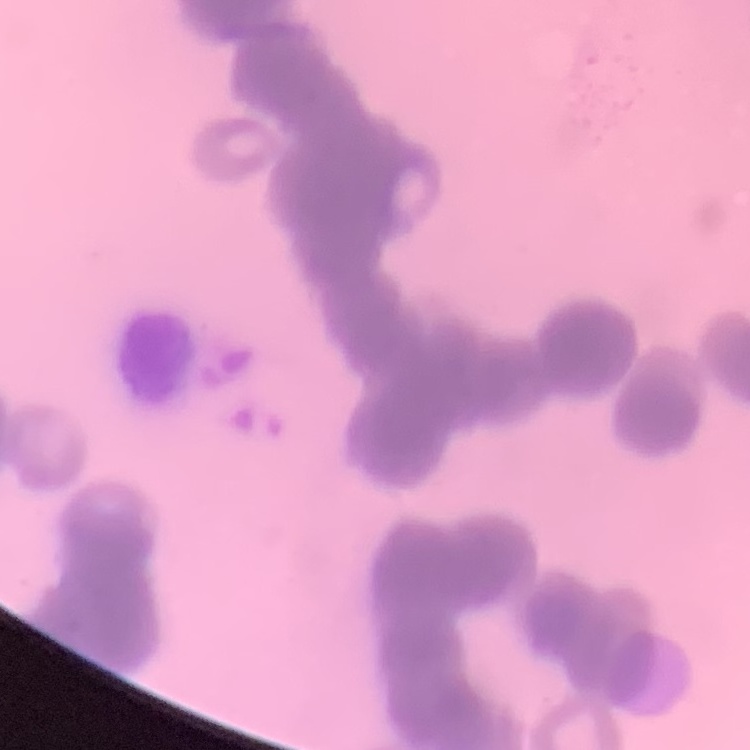

erythrocyte morphology = rouleaux formation
stain = Field's or Giemsa
image type = one tile cut from a larger photomicrograph
preparation = thin peripheral smear